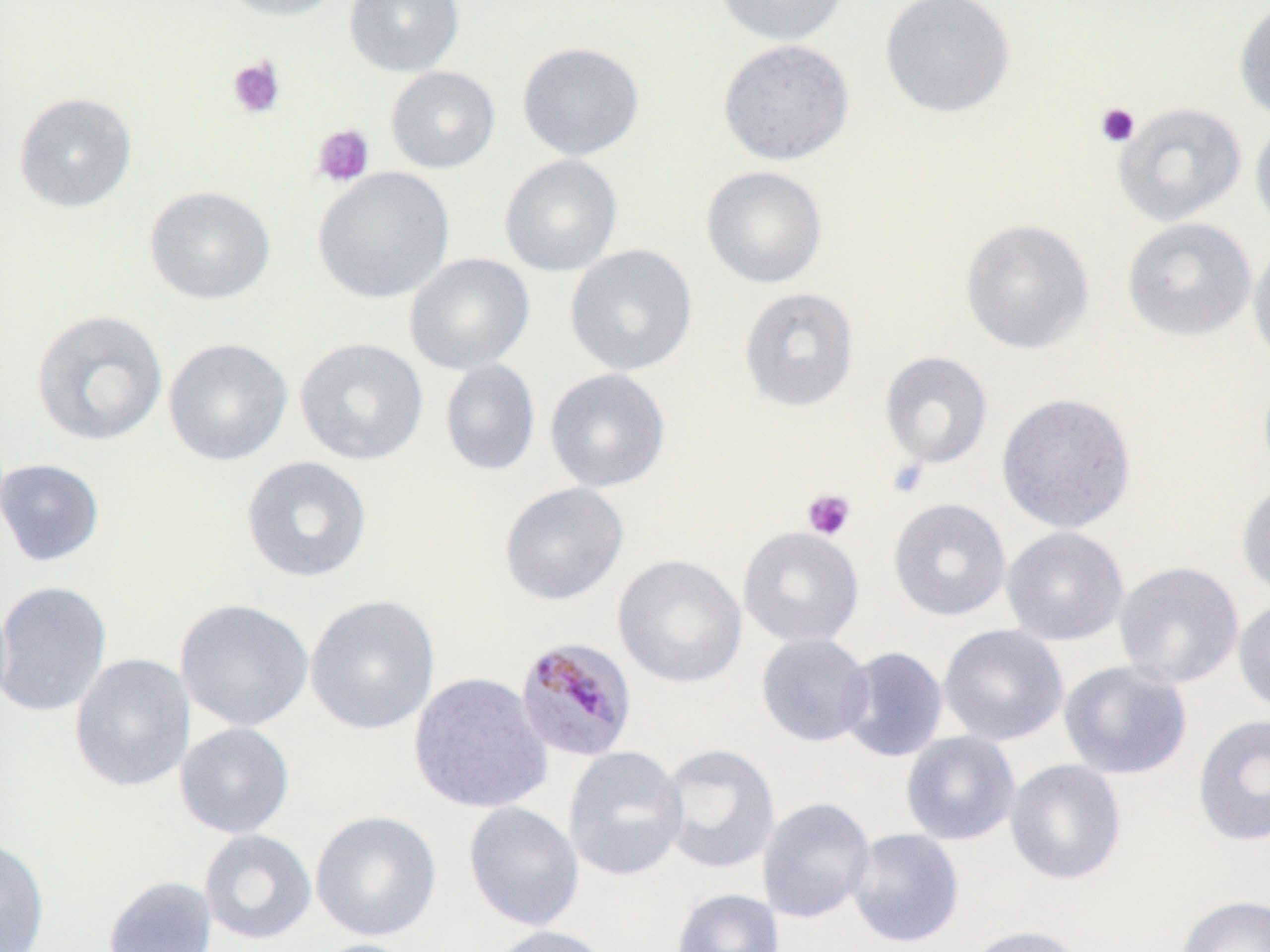
{
  "slide_level_diagnosis": "Plasmodium malariae",
  "stain": "May-Grünwald-Giemsa",
  "modality": "optical microscopy",
  "image_size": "1270×952 pixels",
  "field_of_view": "one of a larger specimen",
  "uninfected_red_blood_cell_locations": "approximate bounding boxes as (x1, y1, x2, y2) in pixels: (215, 0, 347, 21), (344, 0, 465, 77), (713, 0, 850, 46), (879, 0, 1016, 118), (1234, 2, 1270, 125), (717, 38, 854, 165), (516, 41, 645, 161), (385, 66, 501, 173), (13, 92, 137, 212), (1112, 102, 1246, 226), (1250, 118, 1270, 236), (498, 154, 623, 277), (701, 165, 828, 288), (312, 166, 456, 304), (144, 185, 276, 305), (1122, 216, 1257, 341), (959, 218, 1095, 355), (1248, 238, 1270, 369), (565, 243, 698, 376), (404, 252, 535, 375), (738, 287, 860, 412), (31, 308, 169, 447), (162, 337, 293, 466), (294, 337, 428, 466), (879, 351, 993, 469), (439, 359, 541, 476), (544, 367, 671, 492), (996, 392, 1137, 533), (241, 455, 372, 583), (0, 457, 105, 567), (1237, 481, 1270, 601), (499, 482, 629, 605), (888, 497, 1011, 621), (1001, 525, 1130, 646), (738, 526, 865, 648), (612, 554, 748, 689), (1114, 561, 1244, 688), (0, 580, 112, 717), (304, 594, 440, 735), (174, 598, 314, 732), (1233, 598, 1270, 714), (938, 623, 1069, 746), (755, 631, 874, 747), (838, 646, 948, 762), (69, 653, 195, 792), (1059, 660, 1193, 780), (407, 671, 553, 814), (1192, 713, 1270, 847), (174, 722, 295, 839), (900, 731, 1021, 846), (658, 743, 781, 875), (563, 746, 688, 881), (1004, 758, 1127, 885), (757, 796, 875, 924), (462, 801, 584, 932), (310, 810, 442, 941), (198, 828, 317, 945), (845, 828, 965, 948), (0, 837, 50, 951), (102, 875, 218, 952), (670, 887, 785, 952), (1174, 894, 1270, 952), (965, 923, 1086, 952), (485, 925, 615, 952), (305, 939, 424, 952)",
  "preparation": "thin blood film",
  "platelet_locations": "approximate bounding boxes as (x1, y1, x2, y2) in pixels: (226, 56, 286, 120), (1096, 102, 1140, 148), (311, 124, 374, 187), (886, 457, 930, 498), (802, 489, 856, 540)",
  "plasmodium_malariae_infected_red_blood_cell_locations": "approximate bounding boxes as (x1, y1, x2, y2) in pixels: (514, 636, 639, 763)",
  "magnification": "1000x"
}